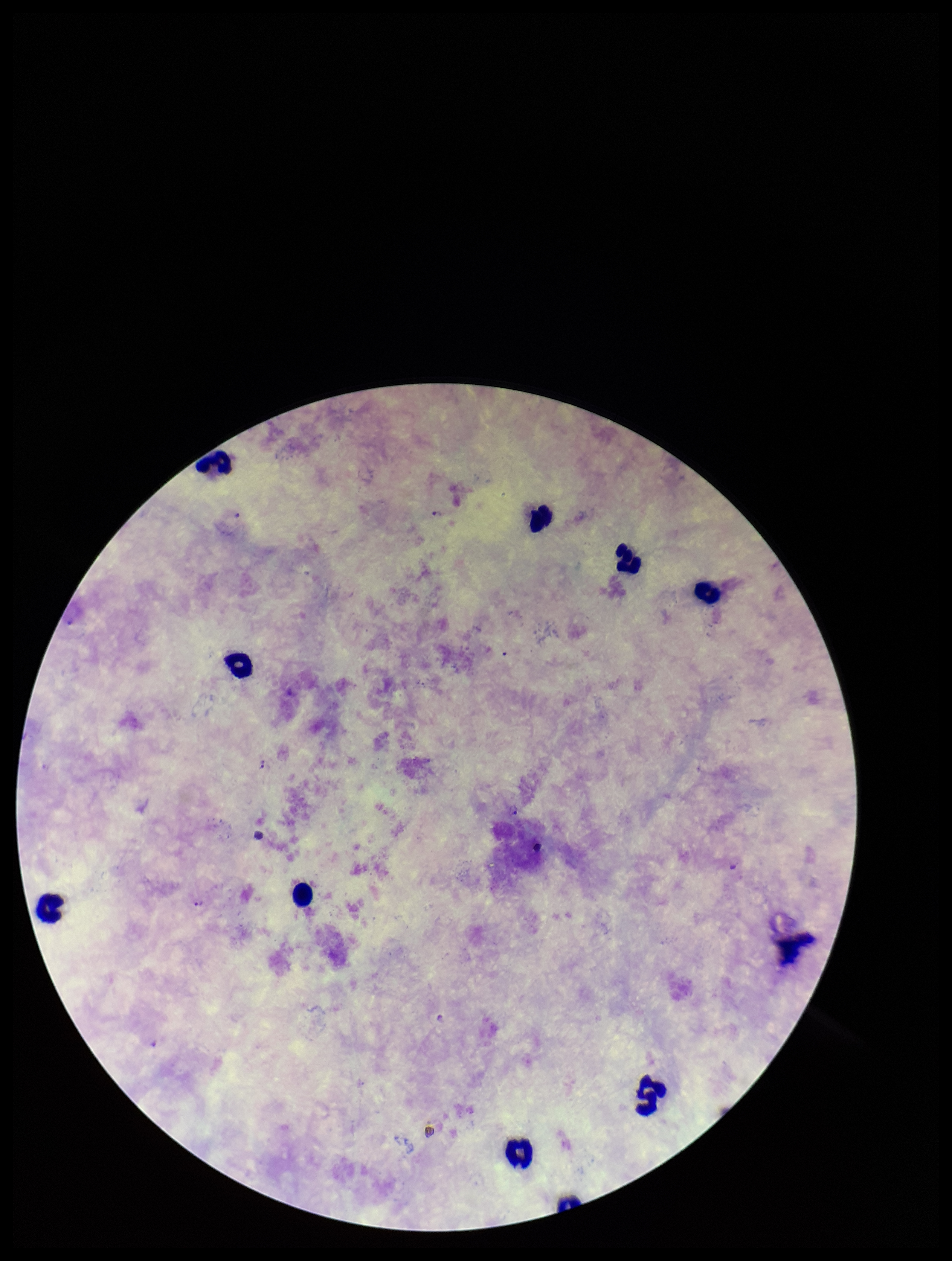

Plasmodium parasites = detected
capture = smartphone photograph through the microscope eyepiece
patient malaria status = infected
preparation = thick
leukocyte count = 11
species reported for this patient = Plasmodium falciparum
stain = Giemsa
field of view = one from this slide
image size = 952×1261 pixels
parasite count = 3